Assess the morphology of the red blood cells.
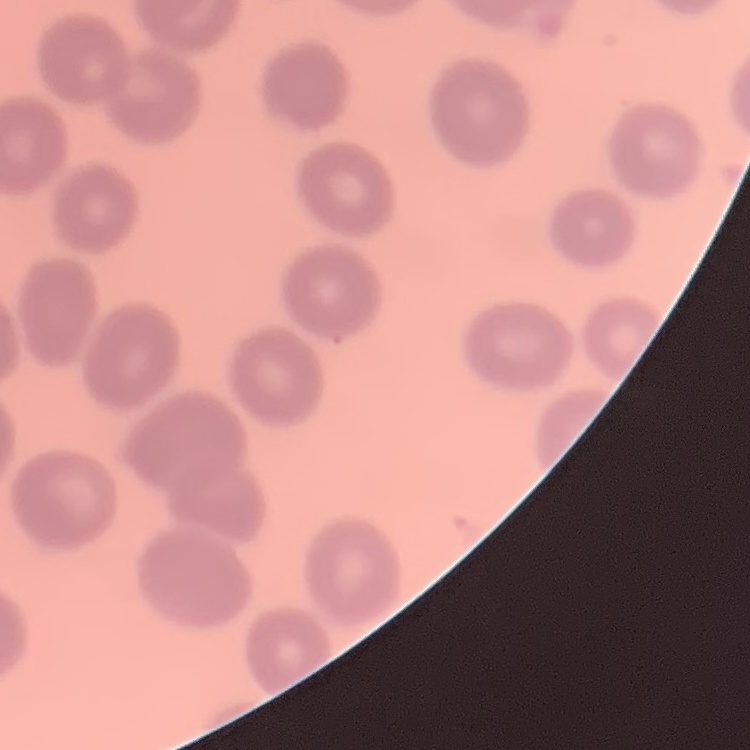
They show no rouleaux formation.

Thin blood smear. Square crop of a larger photomicrograph. Field's or Giemsa stain.